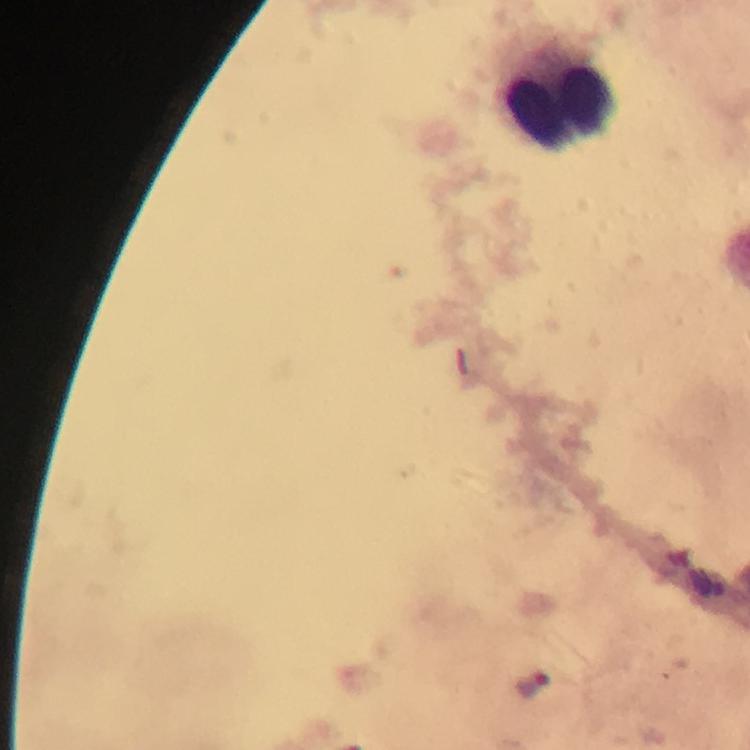 Approximate centers as {x, y} in pixels. Leukocyte locations: {560, 104}. Plasmodium parasite locations: {532, 684}. Image is 750×750 pixels. Smartphone photograph taken through a microscope. Giemsa-stained preparation. Immersion oil was used. A crop from one field of view. Thick blood smear. From a malaria diagnostic workup. At 100x magnification.